Assess the morphology of the red blood cells.
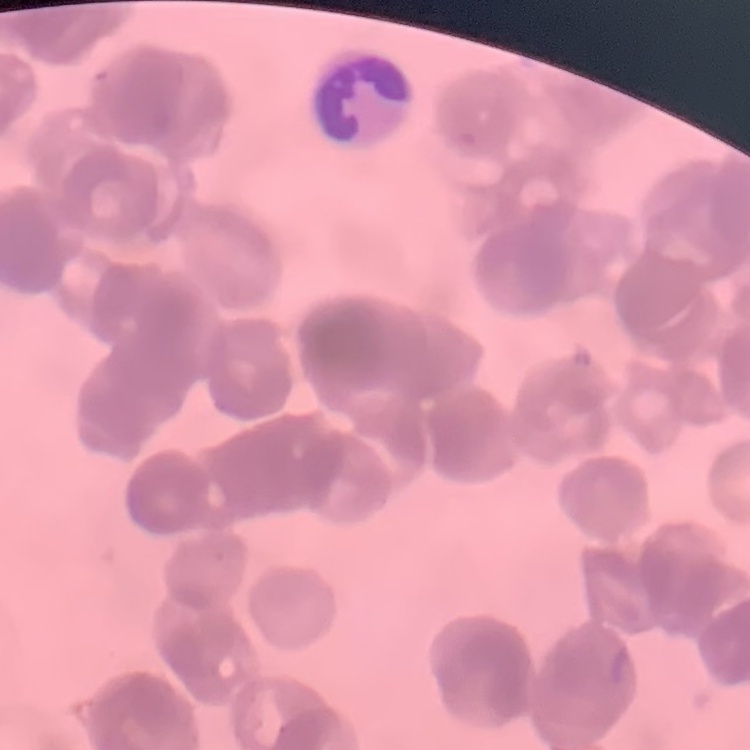
They show rouleaux formation.

{
  "image_type": "one tile cut from a larger photomicrograph",
  "preparation": "thin peripheral smear",
  "stain": "Field's or Giemsa"
}